Give the extent of all Plasmodium ovale-infected red blood cells.
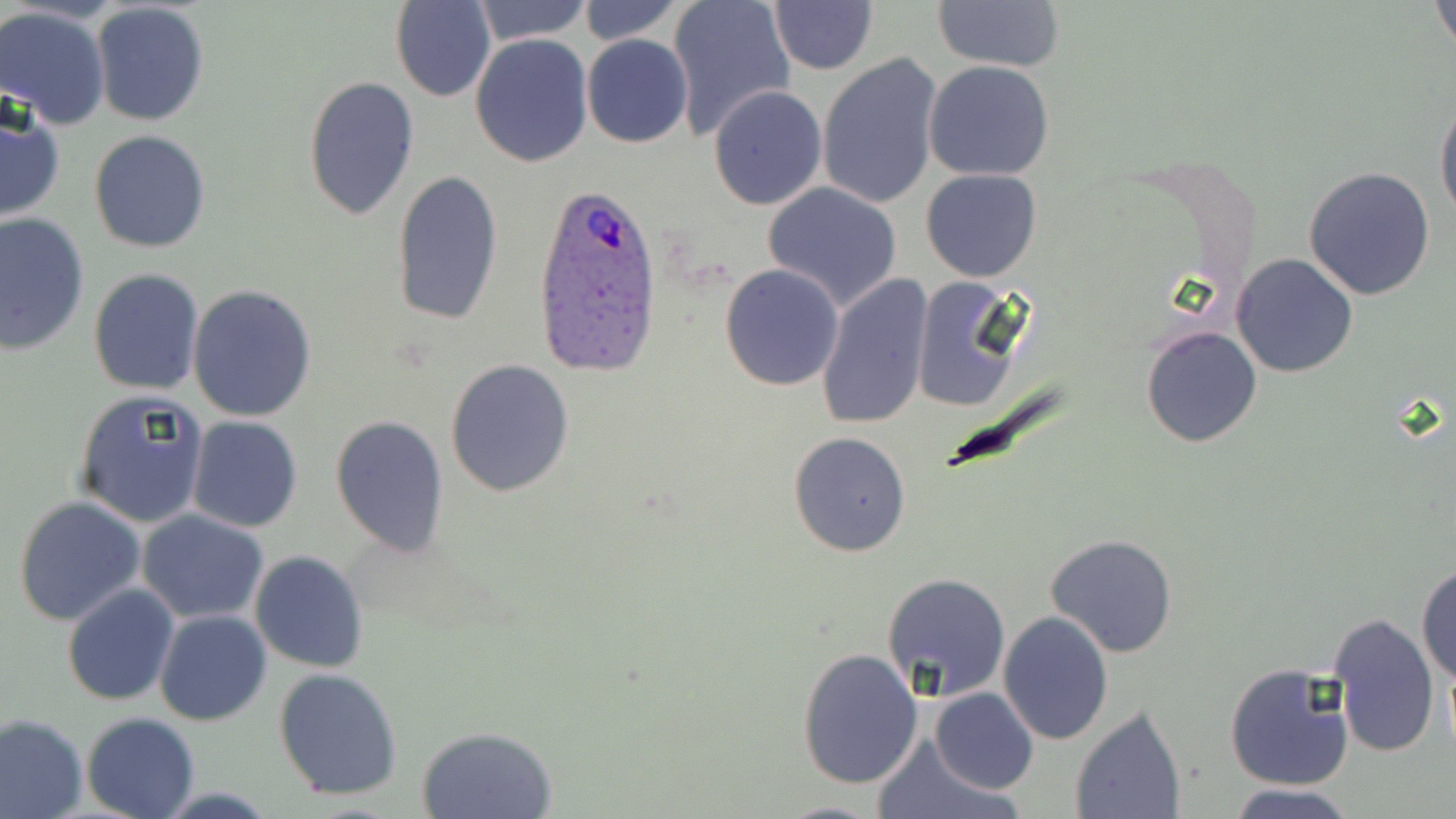

Approximate bounding boxes as (x1,y1)-(x2,y2) corner pairs in pixels.
Plasmodium ovale-infected red blood cells: (535,178)-(663,375).

{
  "slide_level_diagnosis": "Plasmodium ovale",
  "uninfected_red_blood_cell_locations": "approximate bounding boxes as (x1,y1)-(x2,y2) corner pairs in pixels: (392,0)-(496,103), (470,0)-(592,47), (577,0)-(684,46), (666,0)-(796,142), (1432,0)-(1455,58), (91,1)-(210,128), (768,1)-(878,75), (931,1)-(1065,73), (0,6)-(111,130), (581,34)-(693,148), (470,35)-(595,168), (816,52)-(944,210), (924,61)-(1056,183), (301,75)-(419,221), (708,84)-(828,211), (1435,97)-(1456,228), (0,98)-(66,223), (89,129)-(211,253), (1304,166)-(1437,300), (920,167)-(1043,282), (392,168)-(504,327), (761,183)-(903,311), (0,213)-(91,356), (1231,253)-(1358,378), (719,262)-(845,391), (88,267)-(204,394), (814,272)-(934,431), (910,276)-(1026,413), (186,285)-(318,422), (1140,324)-(1262,448), (443,358)-(576,499), (73,389)-(209,528), (330,415)-(449,557), (187,416)-(303,533), (789,430)-(911,557), (13,495)-(146,626), (137,511)-(269,623), (1045,532)-(1177,658), (250,551)-(369,673), (1417,562)-(1456,685), (880,572)-(1011,701), (62,583)-(180,704), (154,610)-(271,727), (999,610)-(1112,743), (1326,610)-(1442,760), (795,647)-(922,789), (1225,662)-(1355,792), (274,668)-(404,799), (932,688)-(1038,795), (1067,704)-(1187,819), (0,713)-(87,819), (80,713)-(199,819), (417,726)-(557,818), (872,735)-(1022,819), (1227,783)-(1360,819), (770,800)-(892,818)",
  "magnification": "1000x",
  "modality": "optical microscopy",
  "field_of_view": "single",
  "image_size": "1456×819 pixels",
  "stain": "May-Grünwald-Giemsa",
  "preparation": "thin blood smear"
}